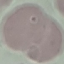 Result: negative for malaria parasites. Thin blood film. Acquired by smartphone through the microscope eyepiece. Automatically extracted cell patch, resized to 64 × 64 pixels. Giemsa stain.